Identify the cell.
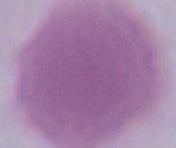
This is an erythrocyte.

Summary:
  - Magnification: 1000x
  - Modality: micrograph